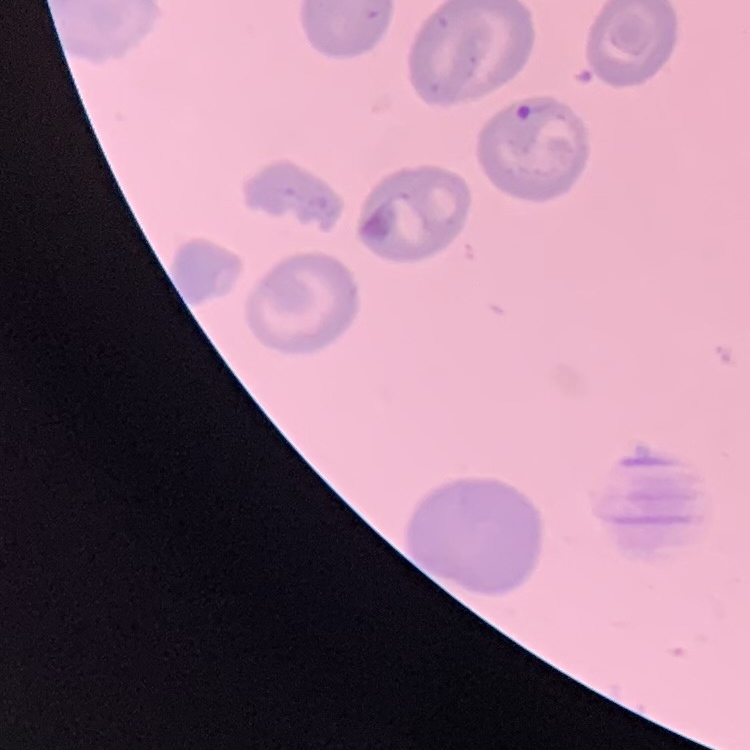 The red blood cells show no rouleaux formation. Stained with either Field's or Giemsa. Square crop of a larger photomicrograph. Thin peripheral smear.